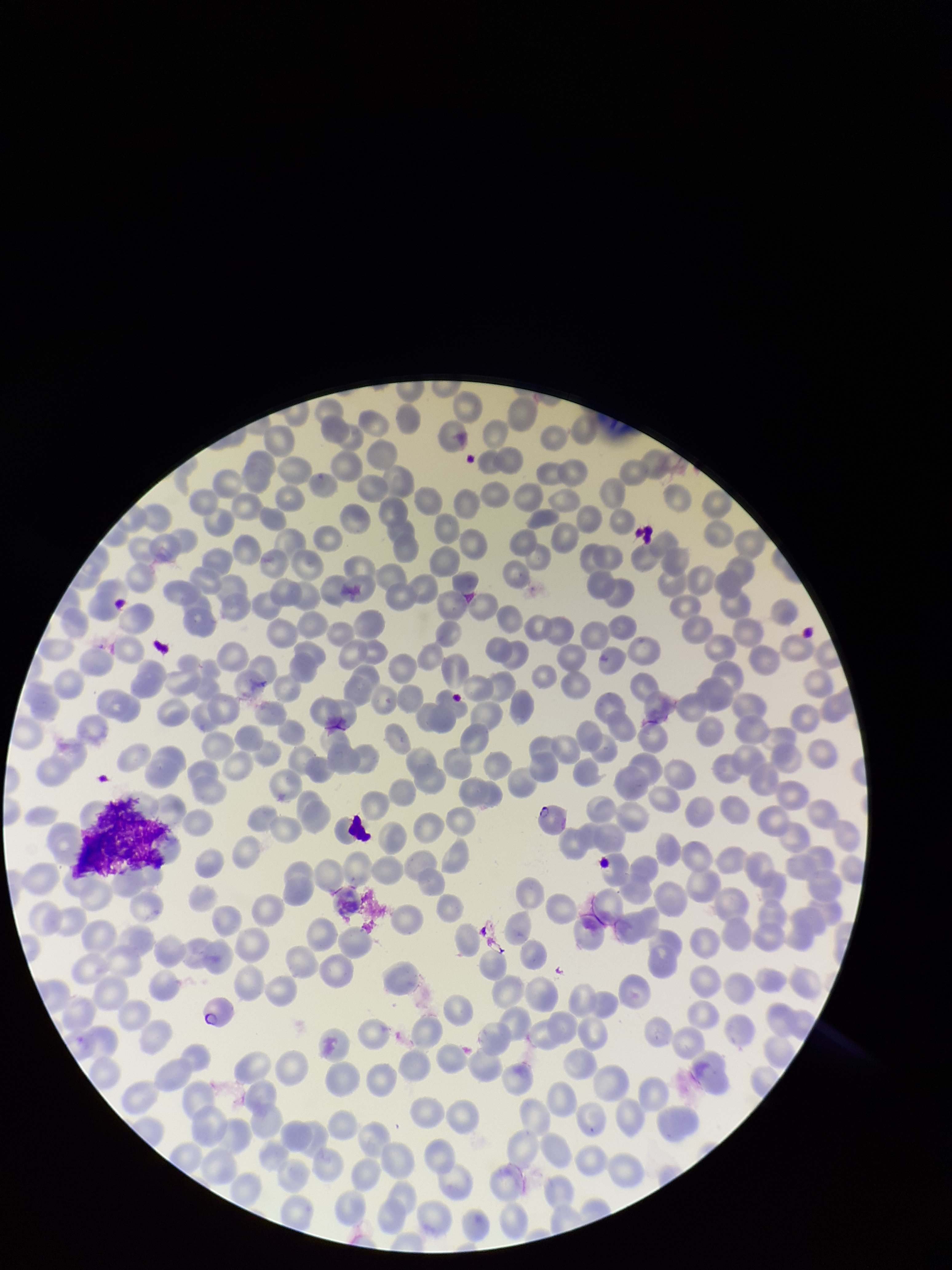
species reported for this patient = Plasmodium falciparum
preparation = thin
parasitized red blood cell count = 0
patient malaria status = positive
stain = Giemsa
red blood cell count = 217
image size = 952×1270 pixels
parasitized red blood cells = none detected
field of view = one from this slide
capture = smartphone photograph through the microscope eyepiece